Classify this cell by malaria status.
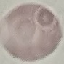
Uninfected.

stain = Giemsa
image type = automatically extracted cell patch, resized to 64 × 64 pixels
capture = smartphone through the microscope eyepiece
preparation = thin blood smear